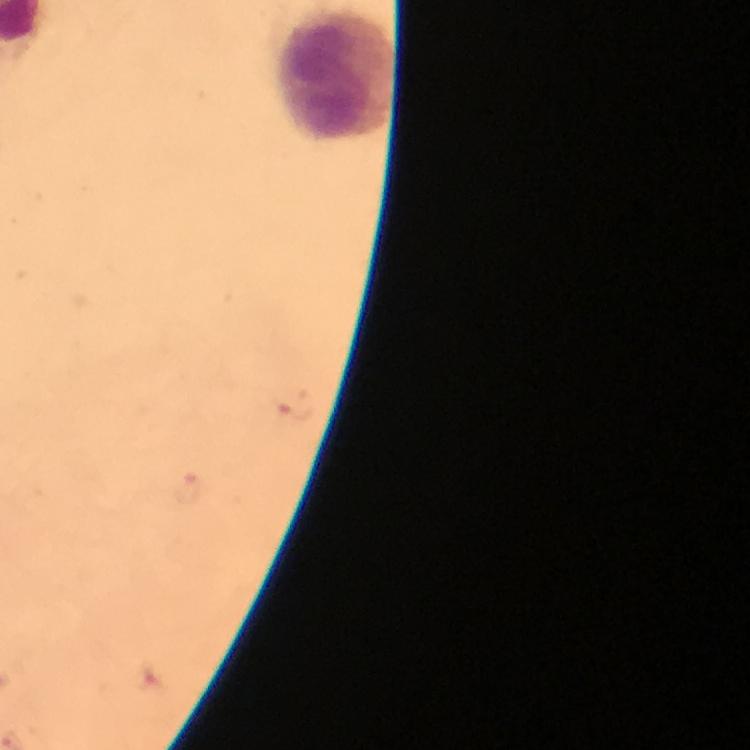
preparation = thick smear
image size = 750×750 pixels
context = from a diagnostic examination for malaria
magnification = 100x
stain = Giemsa
immersion oil = used
cropped from = one field of view
capture = smartphone photograph through a microscope
malaria parasites = none seen
leukocyte locations = approximate centers as {x, y} in pixels: {336, 77}